Describe the morphology of the red blood cells.
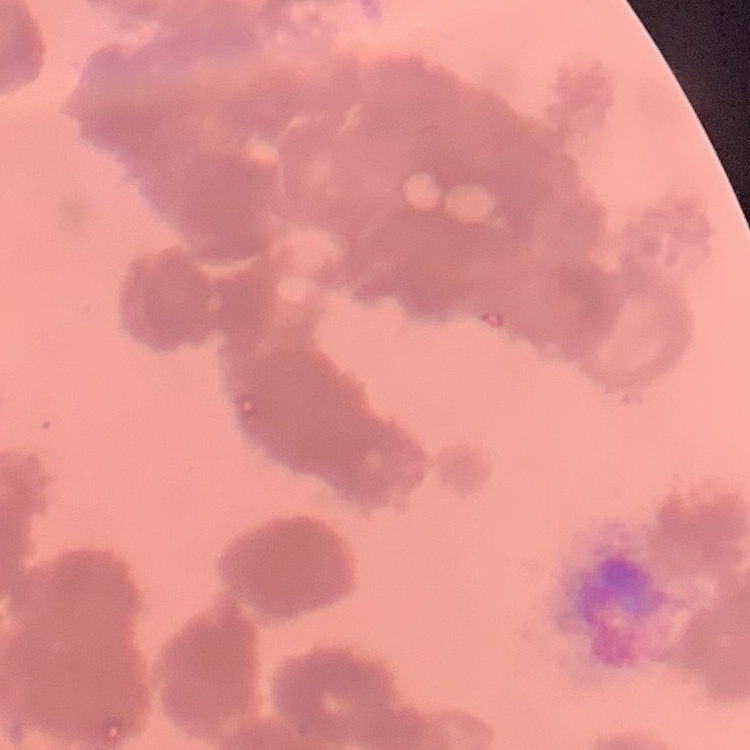

They show rouleaux formation.

stain = Field's or Giemsa
preparation = thin blood film
image type = square crop of a larger photomicrograph